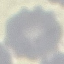
malaria_status: uninfected
capture: smartphone through the microscope eyepiece
stain: Giemsa
image_type: automatically extracted cell patch, resized to 64 × 64 pixels
preparation: thin blood film